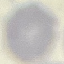

Summary:
  - Result: negative for malaria parasites
  - Capture: smartphone through the microscope eyepiece
  - Preparation: thin blood smear
  - Stain: Giemsa
  - Image type: automatically extracted cell patch, resized to 64 × 64 pixels